Classify this cell by malaria status.
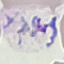

Parasitized.

Summary:
  - Stain: Giemsa
  - Capture: smartphone through the microscope eyepiece
  - Preparation: thin blood film
  - Image type: cell patch, automatically extracted from a larger field of view and resized to 64 × 64 pixels